Give the position of every malaria parasite.
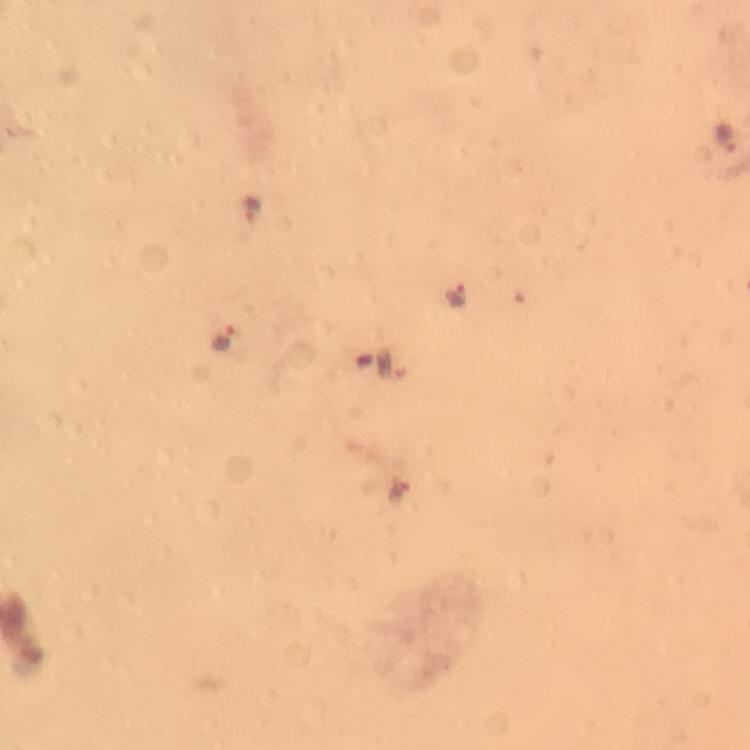
Approximate centers as [x, y] in pixels.
Malaria parasites: [727, 137], [248, 209], [458, 295], [225, 339], [398, 492].

preparation = thick blood film
cropped from = one field of view
stain = Giemsa
immersion oil = used
context = from a malaria diagnostic workup
magnification = 100x
image size = 750×750 pixels
capture = smartphone photograph through a microscope